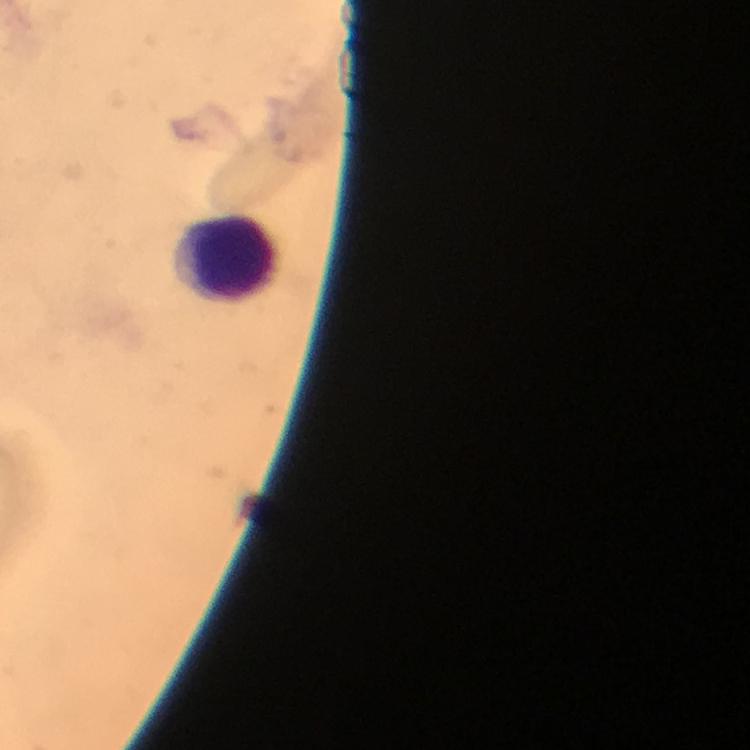 Approximate centers as [x, y] in pixels. Leukocyte locations: [227, 257]. A crop from one field of view. Smartphone photograph taken through a microscope. Image is 750×750 pixels. Giemsa stain. Immersion oil was used. Thick blood film. At 100x magnification. From a malaria diagnostic workup. Plasmodium parasites: none seen.